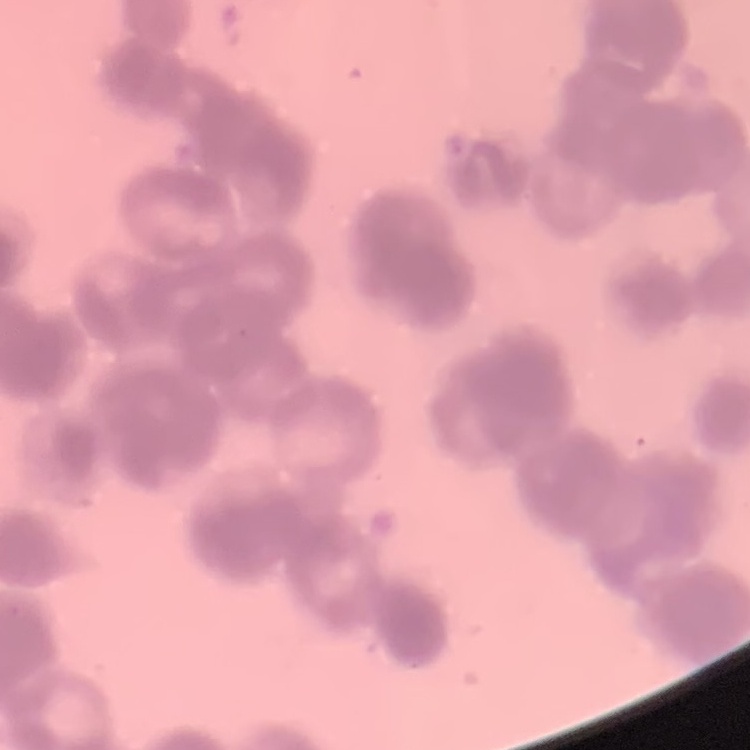
{
  "erythrocyte_morphology": "rouleaux formation",
  "stain": "Field's or Giemsa",
  "preparation": "thin blood film",
  "image_type": "one tile cut from a larger photomicrograph"
}